Outline each blood parasite and name the species.
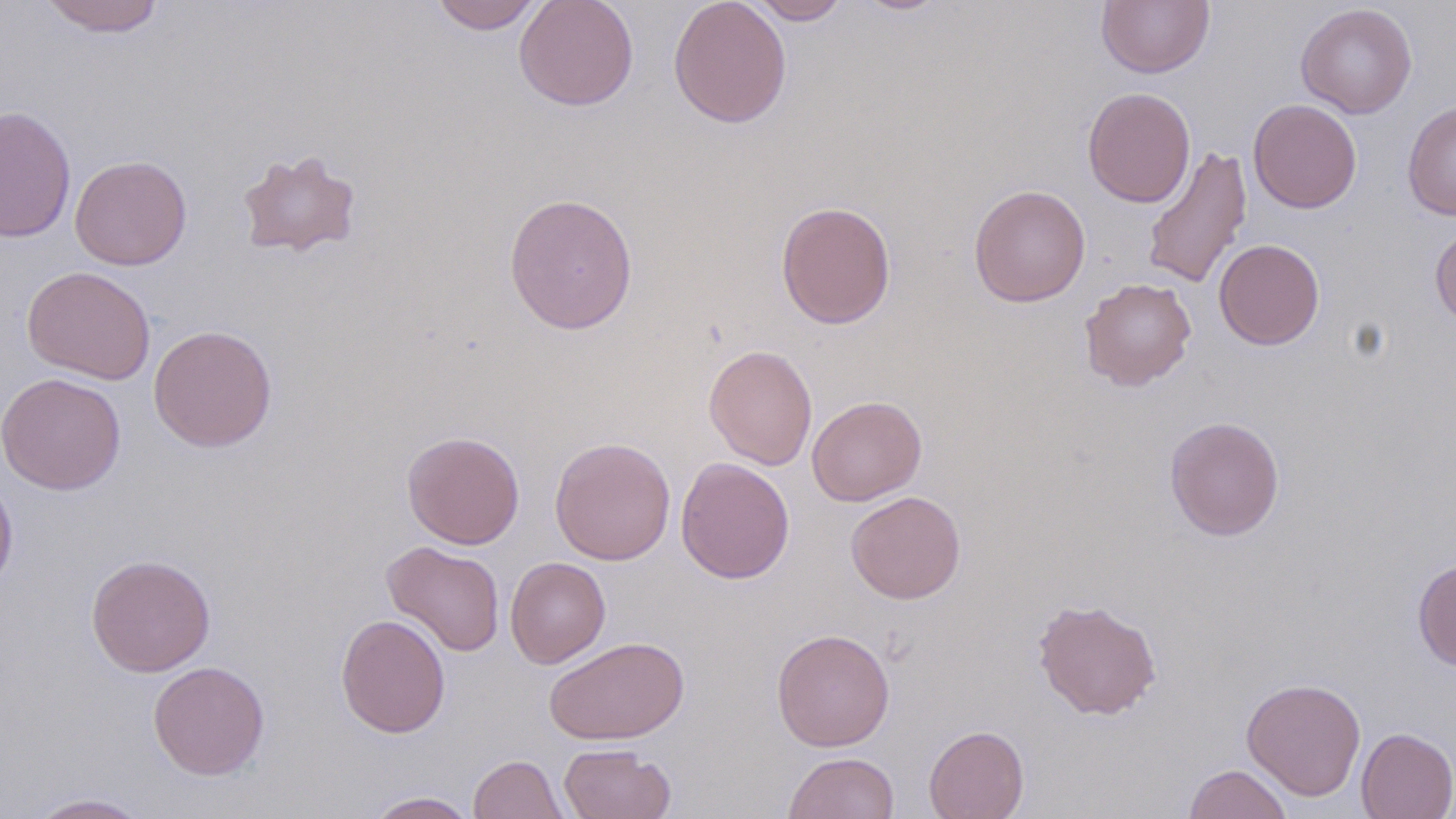

No blood parasites observed.

Summary:
  - Coordinate format: approximate bounding boxes as named x1/y1/x2/y2 corners in pixels
  - Uninfected red blood cell locations: (x1=39, y1=0, x2=166, y2=37), (x1=430, y1=0, x2=544, y2=34), (x1=514, y1=0, x2=639, y2=111), (x1=668, y1=0, x2=792, y2=128), (x1=746, y1=0, x2=851, y2=24), (x1=851, y1=0, x2=953, y2=16), (x1=1096, y1=0, x2=1214, y2=78), (x1=1295, y1=3, x2=1417, y2=118), (x1=1082, y1=86, x2=1196, y2=207), (x1=1247, y1=98, x2=1362, y2=213), (x1=1402, y1=100, x2=1456, y2=220), (x1=0, y1=105, x2=76, y2=244), (x1=1142, y1=144, x2=1252, y2=290), (x1=235, y1=148, x2=363, y2=259), (x1=70, y1=155, x2=192, y2=270), (x1=968, y1=184, x2=1091, y2=307), (x1=503, y1=192, x2=638, y2=335), (x1=776, y1=200, x2=896, y2=329), (x1=1429, y1=223, x2=1456, y2=327), (x1=1214, y1=239, x2=1325, y2=350), (x1=22, y1=265, x2=156, y2=384), (x1=1079, y1=277, x2=1197, y2=390), (x1=148, y1=325, x2=278, y2=452), (x1=703, y1=344, x2=818, y2=470), (x1=0, y1=372, x2=126, y2=494), (x1=807, y1=395, x2=927, y2=506), (x1=1165, y1=415, x2=1285, y2=541), (x1=401, y1=430, x2=524, y2=549), (x1=550, y1=437, x2=676, y2=565), (x1=675, y1=457, x2=795, y2=584), (x1=0, y1=471, x2=18, y2=599), (x1=845, y1=491, x2=966, y2=604), (x1=382, y1=541, x2=505, y2=657), (x1=86, y1=554, x2=216, y2=677), (x1=505, y1=557, x2=610, y2=669), (x1=1412, y1=558, x2=1456, y2=670), (x1=1032, y1=597, x2=1162, y2=720), (x1=336, y1=613, x2=451, y2=738), (x1=771, y1=628, x2=895, y2=751), (x1=544, y1=635, x2=689, y2=745), (x1=147, y1=661, x2=270, y2=780), (x1=1241, y1=677, x2=1366, y2=800), (x1=924, y1=724, x2=1029, y2=819), (x1=1355, y1=727, x2=1456, y2=819), (x1=558, y1=743, x2=675, y2=818), (x1=783, y1=751, x2=900, y2=818), (x1=469, y1=754, x2=568, y2=818), (x1=1183, y1=764, x2=1292, y2=819), (x1=363, y1=791, x2=480, y2=819), (x1=26, y1=793, x2=152, y2=818)
  - Slide-level diagnosis: negative for blood parasites
  - Image size: 1456×819 pixels
  - Field of view: one of a larger specimen
  - Modality: optical microscopy
  - Stain: May-Grünwald-Giemsa
  - Magnification: 1000x
  - Preparation: thin blood smear